Assess this cell for malaria.
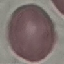

It is uninfected.

Summary:
  - Stain: Giemsa
  - Preparation: thin blood smear
  - Capture: smartphone camera at the microscope eyepiece
  - Image type: automatically extracted cell patch, resized to 64 × 64 pixels